Classify this cell by malaria status.
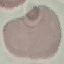
It is uninfected.

Acquired by smartphone through the microscope eyepiece. Thin blood smear. Giemsa stain. Automatically extracted cell patch, resized to 64 × 64 pixels.